Identify the blood parasite species.
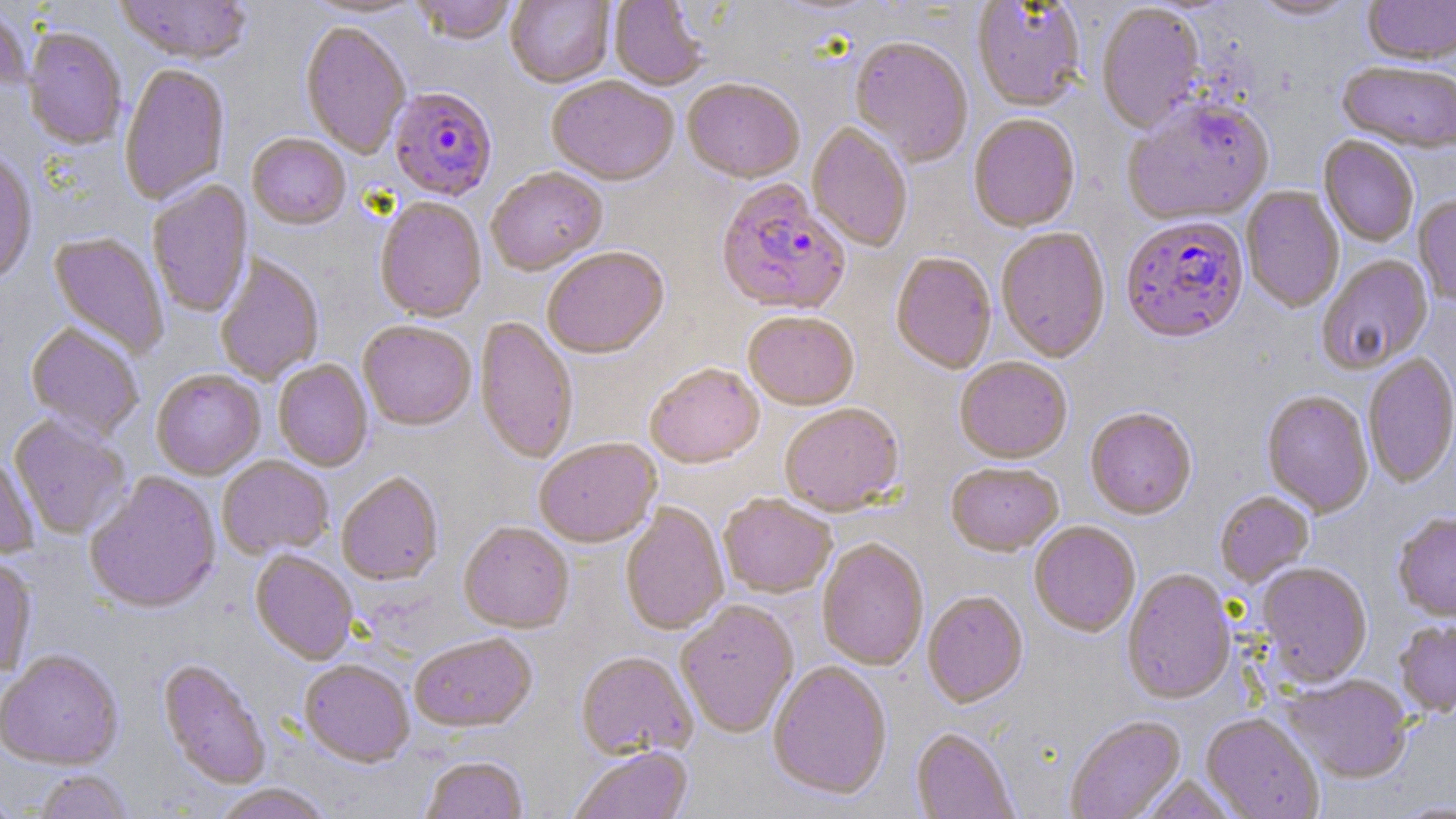
Plasmodium falciparum.

image size = 1456×819 pixels
magnification = 1000x
field of view = one of a larger specimen
uninfected red blood cell locations = approximate bounding boxes as [x1, y1, x2, y2] in pixels: [115, 0, 252, 67], [302, 0, 426, 21], [412, 0, 517, 46], [506, 0, 614, 89], [1248, 0, 1361, 22], [1363, 0, 1456, 67], [609, 1, 706, 92], [972, 1, 1087, 113], [0, 4, 30, 98], [1096, 4, 1206, 135], [299, 24, 411, 160], [23, 29, 127, 151], [850, 39, 973, 168], [1337, 64, 1456, 155], [119, 65, 230, 207], [547, 78, 679, 188], [683, 81, 804, 185], [1121, 98, 1276, 228], [968, 116, 1081, 234], [807, 123, 912, 253], [247, 135, 350, 231], [1318, 137, 1418, 247], [0, 153, 37, 289], [487, 169, 608, 277], [147, 180, 255, 318], [1241, 186, 1344, 314], [1413, 196, 1456, 308], [374, 199, 487, 324], [995, 229, 1110, 364], [48, 232, 169, 359], [542, 249, 670, 361], [891, 254, 996, 375], [215, 255, 325, 387], [1317, 255, 1434, 374], [743, 313, 859, 412], [475, 317, 578, 465], [358, 322, 476, 432], [25, 324, 144, 441], [1363, 355, 1456, 489], [955, 359, 1072, 465], [273, 360, 372, 472], [645, 365, 764, 470], [152, 371, 265, 481], [1262, 392, 1374, 518], [780, 405, 904, 517], [1085, 409, 1196, 521], [9, 415, 131, 539], [534, 439, 662, 550], [0, 453, 39, 560], [218, 457, 334, 560], [946, 464, 1064, 558], [84, 472, 222, 616], [337, 474, 444, 587], [1215, 492, 1315, 589], [718, 494, 836, 599], [620, 503, 729, 636], [1393, 513, 1456, 624], [458, 523, 574, 635], [1029, 523, 1140, 638], [816, 540, 928, 671], [250, 551, 358, 666], [0, 558, 37, 677], [1256, 563, 1373, 688], [1122, 570, 1236, 705], [922, 592, 1028, 709], [676, 602, 798, 738], [1394, 620, 1456, 719], [409, 635, 538, 734], [0, 653, 124, 770], [576, 653, 697, 760], [158, 660, 271, 789], [299, 661, 414, 769], [768, 662, 892, 802], [1280, 675, 1413, 784], [1200, 714, 1324, 819], [1065, 716, 1187, 819], [911, 729, 1019, 818], [570, 748, 692, 819], [420, 757, 528, 819], [33, 770, 133, 819], [1138, 775, 1241, 818], [211, 784, 333, 819], [0, 792, 24, 819]
modality = optical microscopy
Plasmodium falciparum-infected red blood cell locations = approximate bounding boxes as [x1, y1, x2, y2] in pixels: [388, 88, 498, 203], [716, 181, 851, 318], [1120, 217, 1249, 347]
preparation = thin blood smear
stain = May-Grünwald-Giemsa